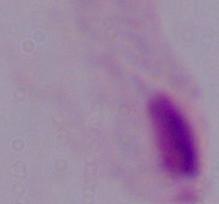
A trichomonad is seen. 1000x magnification. Photomicrograph.